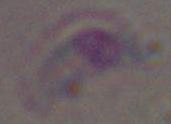

{
  "modality": "micrograph",
  "identification": "Toxoplasma gondii",
  "magnification": "1000x"
}